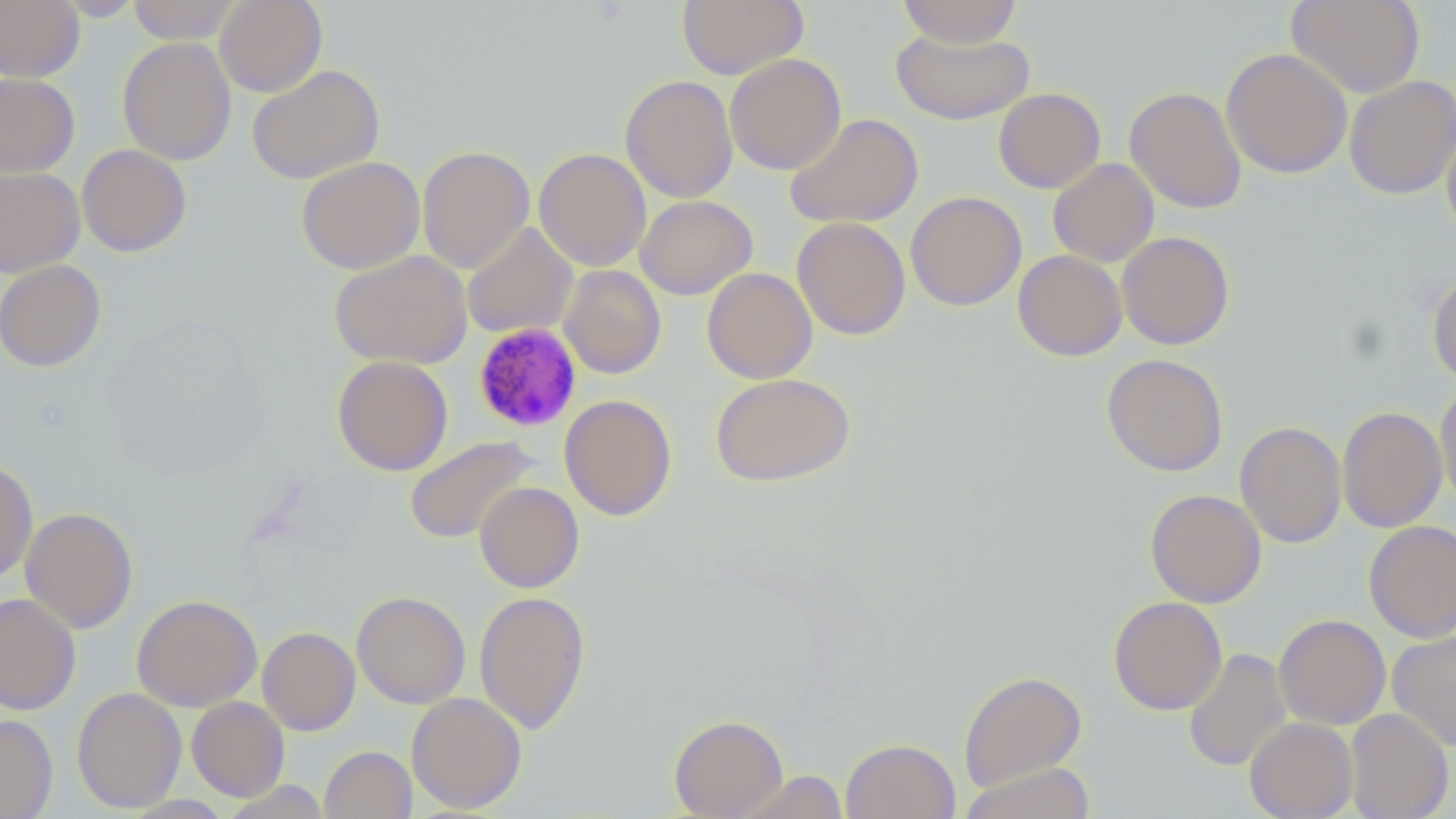 Approximate bounding boxes as (x1, y1, x2, y2) in pixels. Plasmodium malariae-infected red blood cell locations: (472, 322, 583, 433). Uninfected red blood cell locations: (51, 0, 147, 21), (127, 0, 243, 44), (215, 0, 327, 97), (676, 0, 809, 80), (896, 0, 1023, 48), (1286, 0, 1425, 98), (0, 1, 84, 81), (892, 28, 1033, 125), (117, 37, 236, 165), (1221, 48, 1352, 179), (725, 53, 846, 175), (247, 64, 385, 185), (0, 73, 80, 178), (621, 75, 738, 203), (1344, 75, 1456, 200), (1125, 86, 1247, 214), (993, 88, 1106, 194), (785, 113, 923, 228), (1441, 126, 1456, 242), (76, 144, 192, 257), (417, 145, 535, 274), (534, 148, 651, 272), (296, 156, 425, 274), (1048, 158, 1159, 267), (0, 167, 85, 278), (905, 191, 1026, 311), (635, 195, 758, 300), (792, 216, 911, 341), (461, 222, 578, 339), (1117, 231, 1235, 350), (329, 250, 472, 370), (1012, 250, 1127, 361), (0, 260, 106, 372), (558, 265, 666, 379), (702, 267, 816, 384), (1427, 271, 1456, 386), (1101, 354, 1228, 477), (332, 355, 453, 476), (710, 372, 857, 487), (1434, 386, 1456, 508), (559, 394, 677, 521), (1336, 406, 1447, 533), (1234, 421, 1347, 548), (404, 435, 539, 545), (0, 459, 37, 585), (474, 482, 584, 592), (1145, 489, 1266, 607), (20, 506, 138, 634), (1364, 520, 1456, 643), (352, 590, 470, 709), (474, 591, 590, 734), (0, 593, 81, 715), (132, 594, 262, 711), (1108, 596, 1227, 715), (1273, 614, 1391, 730), (258, 626, 360, 735), (1387, 630, 1456, 752), (1183, 648, 1291, 772), (958, 670, 1087, 791), (71, 687, 187, 813), (406, 692, 527, 813), (186, 696, 289, 801), (1344, 708, 1453, 819), (0, 714, 58, 819), (669, 714, 788, 819), (1244, 717, 1357, 818), (840, 738, 960, 819), (320, 745, 416, 819), (959, 762, 1097, 819), (733, 770, 849, 819), (220, 780, 331, 818), (120, 795, 234, 818). Slide-level diagnosis: Plasmodium malariae. Captured at 1000x magnification. Thin blood smear. May-Grünwald-Giemsa stain. Light microscopy. Image is 1456×819 pixels. Single field of view.